Locate and identify every blood parasite.
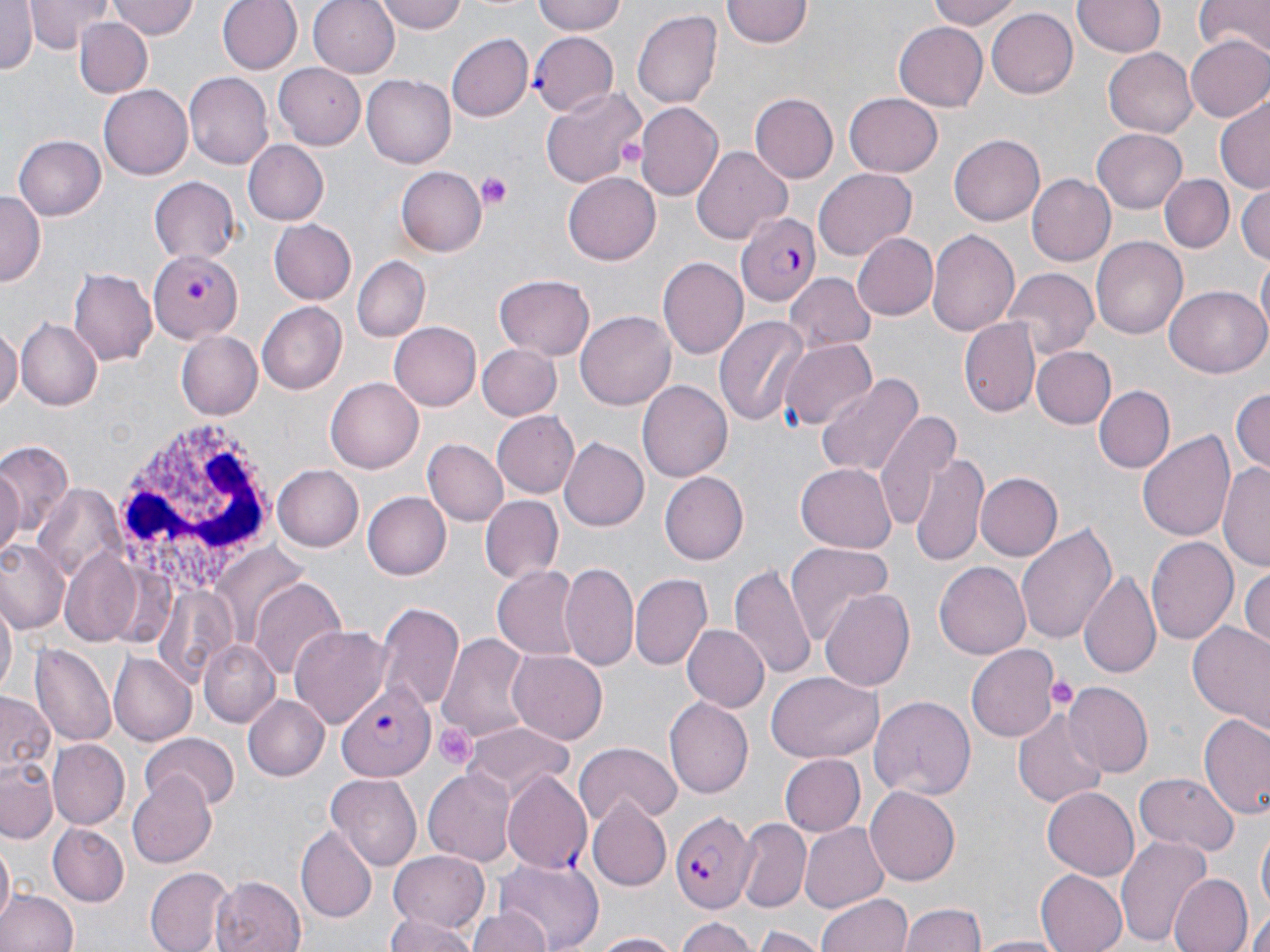

Approximate bounding boxes as [x1, y1, x2, y2] in pixels.
Plasmodium falciparum-infected red blood cells: [530, 32, 618, 114], [737, 210, 822, 308], [148, 252, 241, 341], [335, 680, 438, 780], [501, 771, 593, 875], [672, 811, 755, 912].
No Plasmodium ovale, Plasmodium malariae, Plasmodium vivax, Babesia divergens, or Trypanosoma brucei observed.

Summary:
  - White blood cell locations: [115, 417, 279, 586]
  - Platelet locations: [616, 136, 649, 169], [475, 171, 515, 209], [1048, 675, 1077, 711], [435, 721, 477, 769]
  - Uninfected red blood cell locations: [25, 0, 115, 52], [107, 0, 198, 40], [217, 0, 303, 75], [309, 0, 402, 77], [374, 0, 469, 33], [533, 0, 630, 37], [930, 0, 1023, 31], [1074, 0, 1164, 59], [1195, 0, 1270, 57], [723, 1, 811, 50], [0, 2, 38, 76], [81, 2, 186, 62], [988, 6, 1081, 98], [632, 8, 722, 111], [77, 18, 152, 98], [895, 22, 988, 109], [445, 34, 532, 122], [1184, 34, 1270, 122], [1103, 47, 1197, 137], [276, 63, 369, 147], [184, 73, 273, 170], [361, 75, 455, 168], [541, 84, 647, 191], [100, 86, 193, 179], [1216, 92, 1270, 193], [844, 93, 943, 177], [751, 94, 840, 183], [636, 103, 723, 202], [1091, 129, 1188, 213], [950, 133, 1046, 226], [14, 135, 107, 220], [244, 139, 330, 226], [693, 146, 792, 241], [395, 167, 485, 257], [814, 168, 916, 262], [562, 171, 659, 265], [1026, 171, 1115, 264], [1161, 174, 1231, 252], [148, 176, 241, 265], [1236, 183, 1270, 266], [0, 191, 45, 284], [268, 219, 357, 304], [927, 228, 1021, 339], [850, 232, 938, 321], [1090, 236, 1188, 339], [352, 256, 429, 342], [796, 256, 937, 337], [658, 259, 748, 359], [1003, 268, 1097, 361], [69, 269, 157, 365], [494, 272, 597, 360], [784, 272, 877, 351], [1164, 288, 1268, 377], [257, 302, 348, 394], [577, 311, 676, 411], [714, 315, 809, 427], [15, 317, 102, 411], [960, 317, 1040, 417], [0, 320, 20, 414], [388, 321, 481, 411], [174, 330, 261, 419], [782, 341, 876, 432], [476, 344, 560, 421], [1031, 346, 1116, 428], [814, 373, 923, 481], [325, 377, 423, 473], [637, 380, 732, 483], [1093, 385, 1174, 473], [1231, 385, 1270, 473], [873, 407, 962, 539], [490, 412, 579, 499], [1138, 429, 1236, 545], [560, 436, 652, 531], [424, 440, 509, 527], [0, 441, 74, 552], [911, 453, 988, 568], [1221, 459, 1270, 572], [0, 462, 25, 560], [273, 464, 364, 550], [795, 464, 897, 553], [659, 471, 749, 565], [977, 473, 1065, 561], [361, 491, 450, 580], [480, 495, 563, 585], [1016, 522, 1117, 644], [1146, 536, 1237, 645], [0, 540, 69, 630], [784, 540, 894, 645], [214, 547, 310, 646], [56, 549, 148, 647], [935, 560, 1033, 660], [730, 561, 815, 678], [561, 562, 640, 672], [1240, 564, 1269, 652], [492, 566, 585, 661], [1079, 568, 1162, 683], [630, 573, 710, 671], [249, 580, 347, 681], [821, 587, 915, 693], [1, 596, 16, 701], [376, 601, 464, 713], [291, 624, 392, 730], [680, 625, 767, 712], [1188, 625, 1270, 731], [434, 632, 537, 750], [200, 641, 279, 724], [29, 645, 116, 749], [965, 645, 1061, 744], [507, 649, 609, 745], [107, 651, 195, 745], [765, 673, 884, 764], [1060, 682, 1152, 776], [0, 692, 58, 779], [244, 694, 332, 782], [869, 694, 976, 801], [663, 696, 752, 799], [1012, 704, 1107, 812], [1198, 711, 1270, 821], [464, 723, 574, 797], [138, 735, 239, 809], [47, 740, 130, 831], [573, 743, 682, 828], [778, 754, 864, 837], [0, 757, 60, 842], [423, 769, 516, 867], [128, 771, 217, 870], [1136, 771, 1238, 857], [327, 774, 423, 870], [866, 786, 960, 887], [1041, 787, 1139, 882], [587, 800, 671, 891], [739, 820, 810, 909], [800, 821, 890, 914], [48, 823, 128, 905], [1256, 825, 1269, 921], [297, 826, 376, 920], [1115, 833, 1212, 946], [1, 843, 13, 929], [390, 851, 488, 933], [497, 861, 604, 950], [146, 867, 231, 951], [1036, 868, 1131, 952], [213, 874, 307, 952], [1168, 874, 1252, 952], [0, 889, 76, 952], [818, 893, 913, 952], [466, 905, 555, 952], [901, 905, 987, 952], [383, 910, 478, 952], [1246, 910, 1270, 952], [674, 917, 758, 952], [754, 923, 825, 952], [584, 932, 685, 951], [975, 934, 1070, 952]
  - Slide-level diagnosis: Plasmodium falciparum
  - Field of view: one of a larger specimen
  - Stain: May-Grünwald-Giemsa
  - Modality: light microscopy
  - Image size: 1270×952 pixels
  - Magnification: 1000x
  - Preparation: thin blood film